Name the cell type shown.
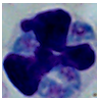
A leukocyte.

Summary:
  - Modality: photomicrograph
  - Magnification: 1000x